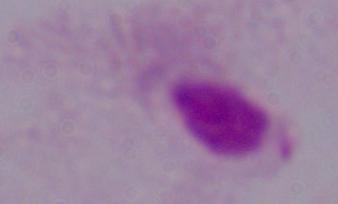 A trichomonad is shown. 1000x magnification. Photomicrograph.